Outline each blood parasite and name the species.
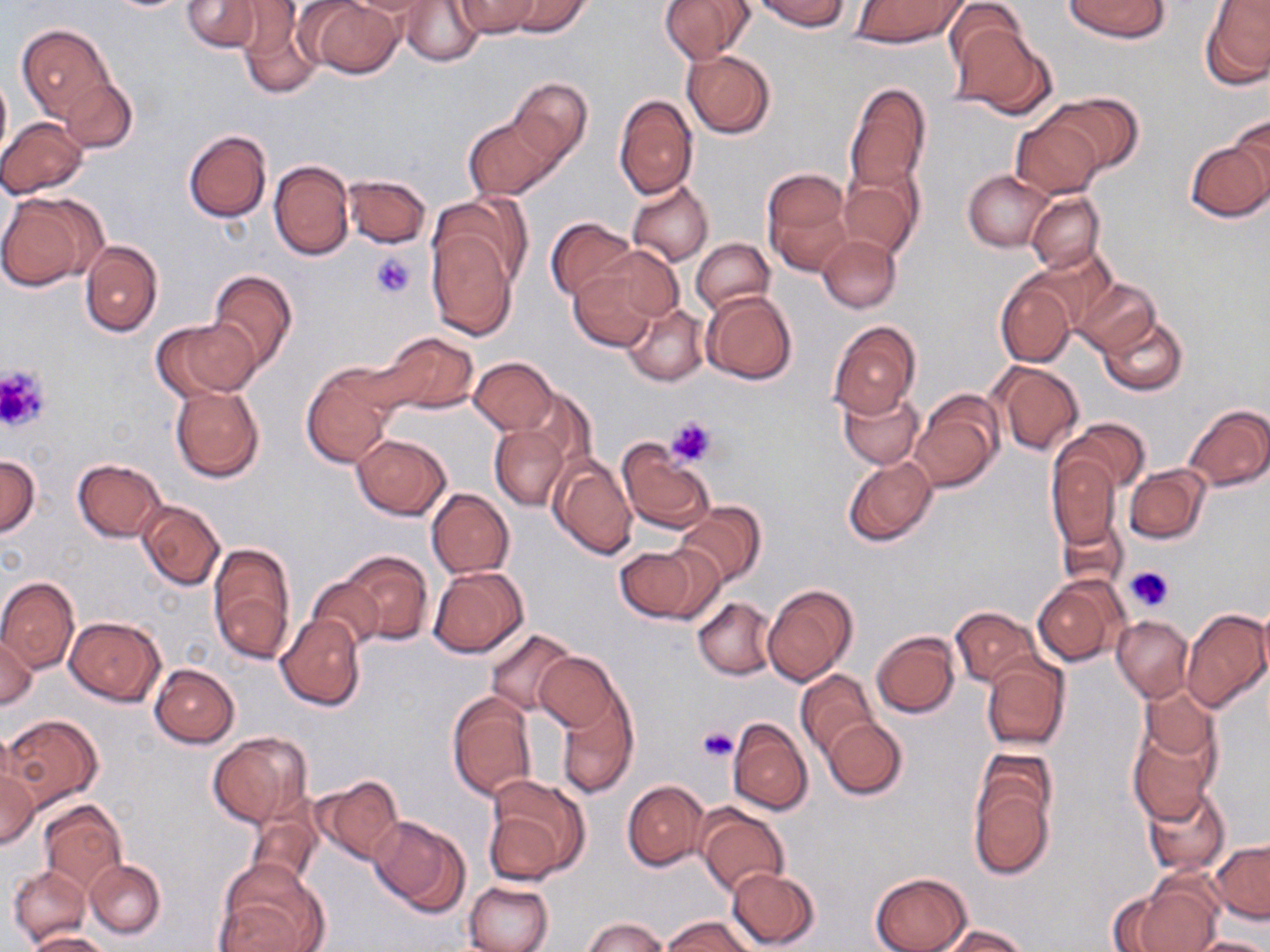

No blood parasites seen.

Summary:
  - Coordinate format: approximate bounding boxes as (x1, y1, x2, y2) in pixels
  - Uninfected red blood cell locations: (181, 0, 262, 53), (184, 0, 312, 70), (304, 0, 403, 80), (342, 0, 440, 18), (453, 0, 540, 37), (508, 0, 591, 37), (659, 0, 755, 64), (755, 0, 850, 31), (1065, 0, 1167, 41), (401, 1, 484, 66), (850, 1, 966, 48), (943, 1, 1029, 78), (1201, 2, 1270, 88), (236, 8, 322, 98), (16, 23, 114, 123), (951, 25, 1055, 119), (681, 50, 775, 138), (0, 69, 10, 162), (59, 76, 136, 153), (507, 78, 592, 168), (844, 81, 932, 194), (1047, 93, 1140, 173), (613, 95, 697, 198), (463, 113, 560, 202), (1228, 115, 1270, 203), (1011, 116, 1104, 198), (1, 118, 89, 198), (183, 130, 271, 222), (1183, 137, 1270, 222), (268, 160, 355, 261), (762, 169, 852, 274), (964, 170, 1052, 251), (839, 172, 921, 258), (342, 174, 431, 248), (627, 181, 713, 268), (0, 192, 106, 292), (1026, 193, 1103, 272), (434, 194, 532, 288), (544, 216, 636, 303), (425, 229, 517, 339), (818, 234, 901, 312), (692, 238, 774, 315), (80, 241, 163, 336), (597, 247, 684, 325), (1025, 250, 1117, 332), (570, 266, 659, 351), (207, 270, 298, 373), (995, 277, 1077, 367), (1074, 278, 1158, 356), (700, 290, 798, 385), (622, 302, 709, 387), (1098, 315, 1188, 396), (154, 317, 260, 399), (827, 321, 920, 418), (379, 332, 478, 417), (469, 356, 557, 434), (991, 362, 1085, 455), (301, 365, 397, 468), (170, 385, 264, 482), (516, 386, 594, 474), (838, 389, 923, 469), (911, 390, 1004, 492), (1183, 404, 1270, 491), (1060, 418, 1150, 494), (489, 424, 568, 510), (352, 434, 450, 519), (617, 441, 714, 533), (1047, 451, 1123, 552), (0, 455, 40, 537), (548, 455, 637, 562), (843, 457, 937, 548), (72, 459, 165, 543), (1124, 465, 1210, 545), (426, 489, 514, 578), (136, 500, 225, 590), (674, 503, 766, 588), (1057, 514, 1128, 591), (208, 542, 297, 663), (615, 544, 711, 624), (339, 551, 432, 645), (429, 566, 528, 659), (0, 576, 79, 672), (308, 576, 383, 652), (1034, 577, 1125, 666), (763, 584, 857, 684), (692, 598, 777, 679), (1256, 606, 1270, 687), (950, 607, 1039, 687), (1181, 609, 1269, 713), (276, 614, 366, 711), (1111, 615, 1193, 701), (65, 616, 165, 706), (485, 629, 577, 715), (872, 631, 961, 717), (0, 634, 38, 710), (534, 652, 621, 733), (981, 659, 1070, 752), (149, 664, 240, 748), (796, 669, 878, 759), (1139, 687, 1219, 766), (446, 692, 537, 801), (553, 694, 638, 799), (3, 715, 103, 808), (727, 718, 812, 815), (821, 718, 906, 800), (1128, 725, 1219, 822), (208, 732, 309, 827), (974, 748, 1057, 833), (0, 765, 38, 851), (313, 776, 403, 865), (485, 777, 587, 882), (623, 781, 709, 870), (969, 783, 1054, 879), (1143, 784, 1231, 875), (41, 801, 126, 892), (247, 804, 324, 891), (696, 807, 789, 897), (369, 814, 471, 917), (1210, 839, 1269, 922), (84, 859, 165, 939), (8, 865, 91, 945), (216, 865, 326, 951), (726, 866, 819, 950), (870, 873, 970, 952), (1120, 878, 1223, 952), (465, 882, 552, 952), (664, 915, 753, 952), (583, 917, 667, 952), (935, 925, 1032, 952), (25, 930, 108, 952), (1188, 936, 1270, 952)
  - Platelet locations: (370, 251, 416, 299), (0, 364, 50, 434), (666, 415, 717, 466), (1125, 564, 1175, 613), (697, 727, 737, 764)
  - Slide-level diagnosis: negative for blood parasites
  - Field of view: single
  - Preparation: thin blood film
  - Image size: 1270×952 pixels
  - Magnification: 1000x
  - Stain: May-Grünwald-Giemsa
  - Modality: light microscopy